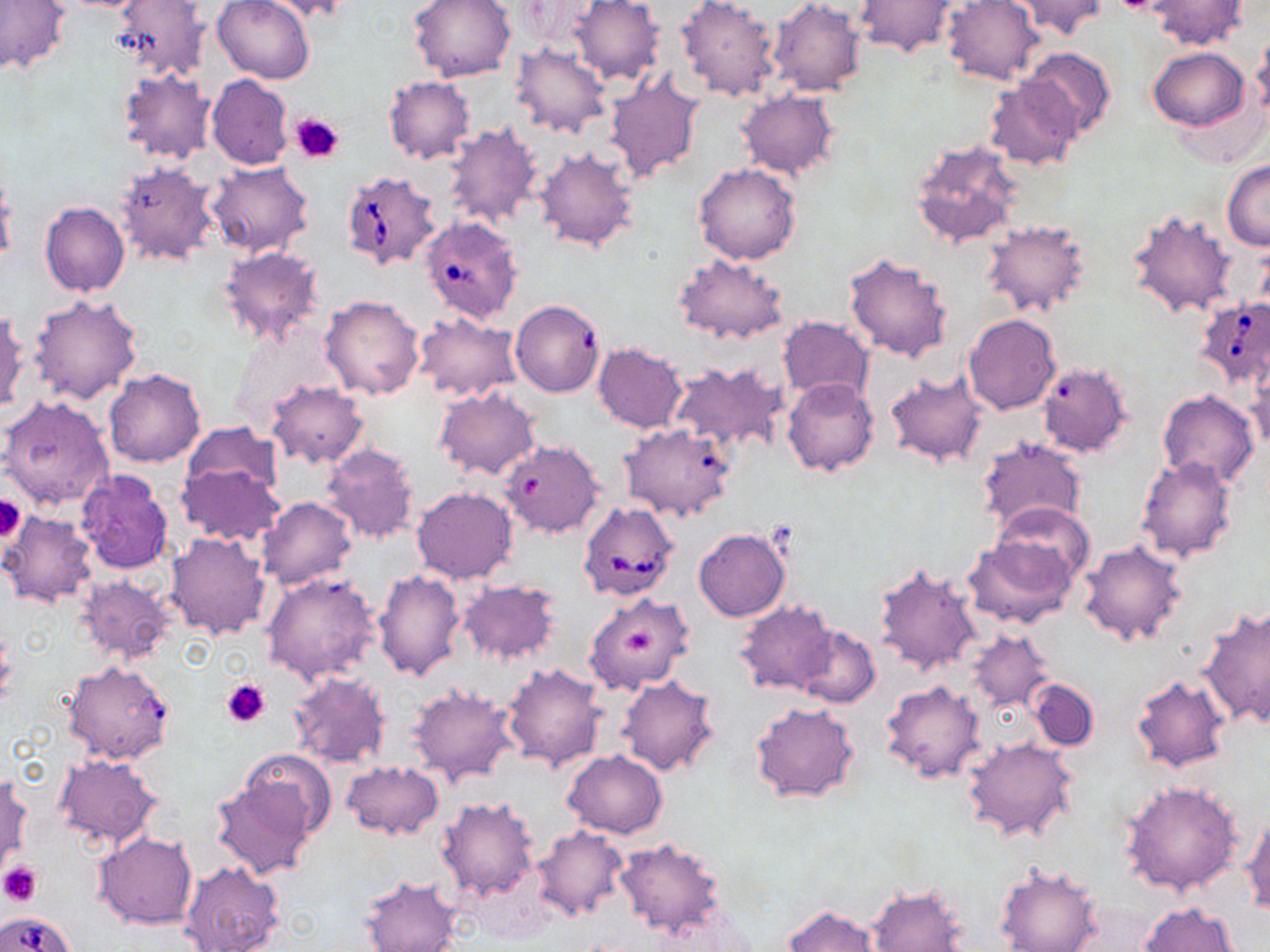

Approximate bounding boxes as (x1, y1, x2, y2) in pixels. Platelet locations: (291, 112, 345, 164), (0, 492, 24, 545), (624, 628, 653, 658), (222, 678, 270, 728), (0, 861, 42, 905). Uninfected red blood cell locations: (0, 0, 69, 75), (112, 0, 209, 83), (212, 0, 315, 83), (260, 0, 355, 21), (409, 0, 517, 82), (568, 0, 665, 87), (675, 0, 781, 102), (768, 0, 867, 97), (942, 0, 1044, 86), (1011, 0, 1108, 40), (1150, 0, 1247, 49), (513, 1, 606, 48), (852, 1, 961, 57), (1249, 34, 1270, 128), (511, 43, 611, 137), (1020, 46, 1116, 139), (1149, 47, 1250, 130), (116, 68, 217, 166), (604, 72, 705, 182), (206, 74, 293, 170), (383, 76, 476, 165), (984, 77, 1083, 170), (737, 90, 839, 179), (444, 122, 544, 230), (911, 137, 1023, 249), (533, 147, 640, 252), (1222, 160, 1270, 250), (113, 161, 221, 267), (206, 162, 315, 258), (694, 164, 802, 266), (0, 181, 16, 272), (39, 202, 130, 297), (1126, 206, 1239, 320), (980, 220, 1092, 318), (216, 245, 325, 347), (843, 250, 954, 363), (673, 253, 789, 343), (29, 294, 143, 404), (320, 294, 425, 401), (514, 305, 604, 396), (0, 310, 27, 415), (413, 313, 523, 404), (964, 313, 1060, 414), (777, 315, 874, 401), (593, 342, 687, 433), (1037, 361, 1134, 457), (666, 362, 787, 454), (1246, 362, 1270, 453), (103, 368, 205, 467), (883, 370, 988, 468), (783, 379, 878, 476), (267, 381, 368, 468), (434, 387, 539, 479), (1158, 390, 1259, 487), (2, 396, 115, 510), (180, 423, 283, 504), (623, 430, 735, 522), (976, 437, 1087, 536), (499, 439, 603, 539), (321, 442, 420, 547), (1136, 456, 1238, 561), (176, 461, 285, 548), (76, 468, 173, 574), (411, 487, 518, 584), (256, 496, 357, 591), (993, 503, 1094, 584), (0, 510, 99, 608), (694, 528, 790, 621), (166, 532, 270, 639), (964, 536, 1079, 630), (1079, 540, 1188, 647), (874, 562, 983, 675), (374, 571, 466, 682), (260, 572, 383, 685), (74, 575, 175, 665), (458, 580, 561, 667), (584, 592, 694, 695), (734, 599, 840, 696), (1199, 604, 1270, 729), (793, 626, 880, 709), (965, 628, 1054, 712), (62, 659, 175, 764), (502, 662, 607, 772), (289, 671, 391, 769), (617, 673, 720, 777), (1131, 674, 1232, 773), (1026, 679, 1100, 751), (881, 680, 987, 783), (408, 684, 521, 788), (750, 701, 859, 805), (962, 736, 1079, 844), (562, 750, 668, 838), (238, 751, 337, 839), (51, 754, 161, 852), (341, 760, 443, 839), (1, 770, 31, 873), (210, 778, 316, 880), (1118, 778, 1245, 896), (434, 796, 540, 901), (1241, 813, 1270, 914), (533, 826, 630, 921), (93, 832, 198, 930), (613, 838, 728, 935), (180, 861, 285, 952), (994, 862, 1103, 952), (358, 876, 461, 952), (866, 884, 970, 951), (1137, 902, 1239, 952), (782, 904, 885, 952). Babesia divergens-infected red blood cell locations: (340, 172, 442, 271), (420, 221, 520, 321), (1194, 296, 1270, 385), (577, 501, 678, 602), (4, 911, 74, 952). Slide-level diagnosis: Babesia divergens. Thin blood film. Optical microscopy. 1000x magnification. May-Grünwald-Giemsa stain. Single field of view. Image is 1270×952 pixels.